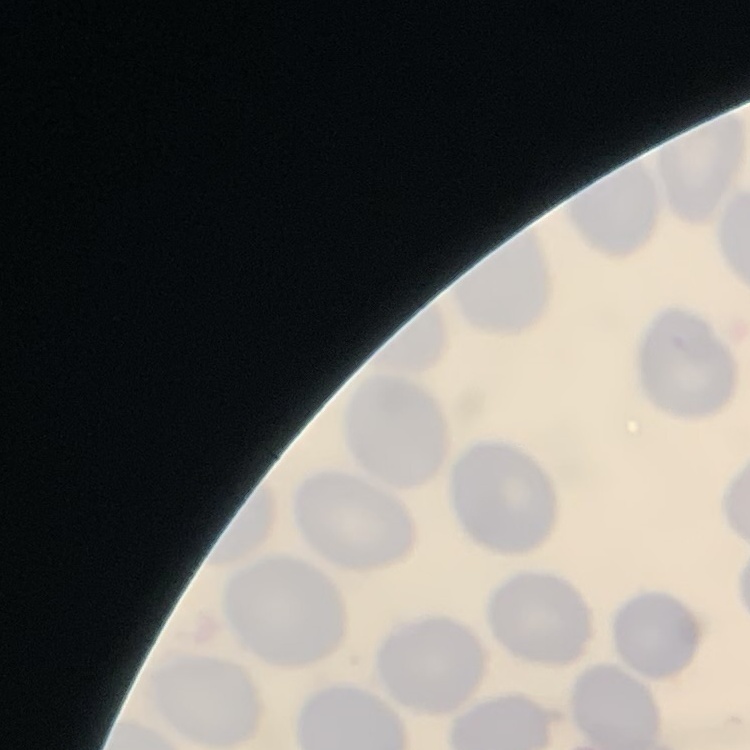
Summary:
  - Red blood cell morphology: no rouleaux formation
  - Preparation: thin peripheral smear
  - Stain: Field's or Giemsa
  - Image type: square crop of a larger photomicrograph